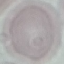
Summary:
  - Result: no malaria parasites detected
  - Image type: cell patch, automatically extracted from a larger field of view and resized to 64 × 64 pixels
  - Stain: Giemsa
  - Capture: smartphone camera at the microscope eyepiece
  - Preparation: thin smear